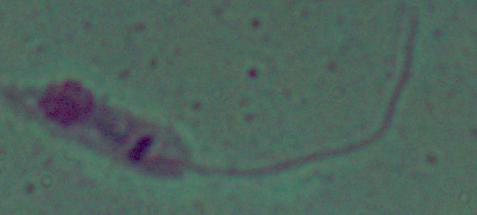

A Leishmania parasite is seen. Captured at 1000x magnification. Photomicrograph.